State the blood parasite species.
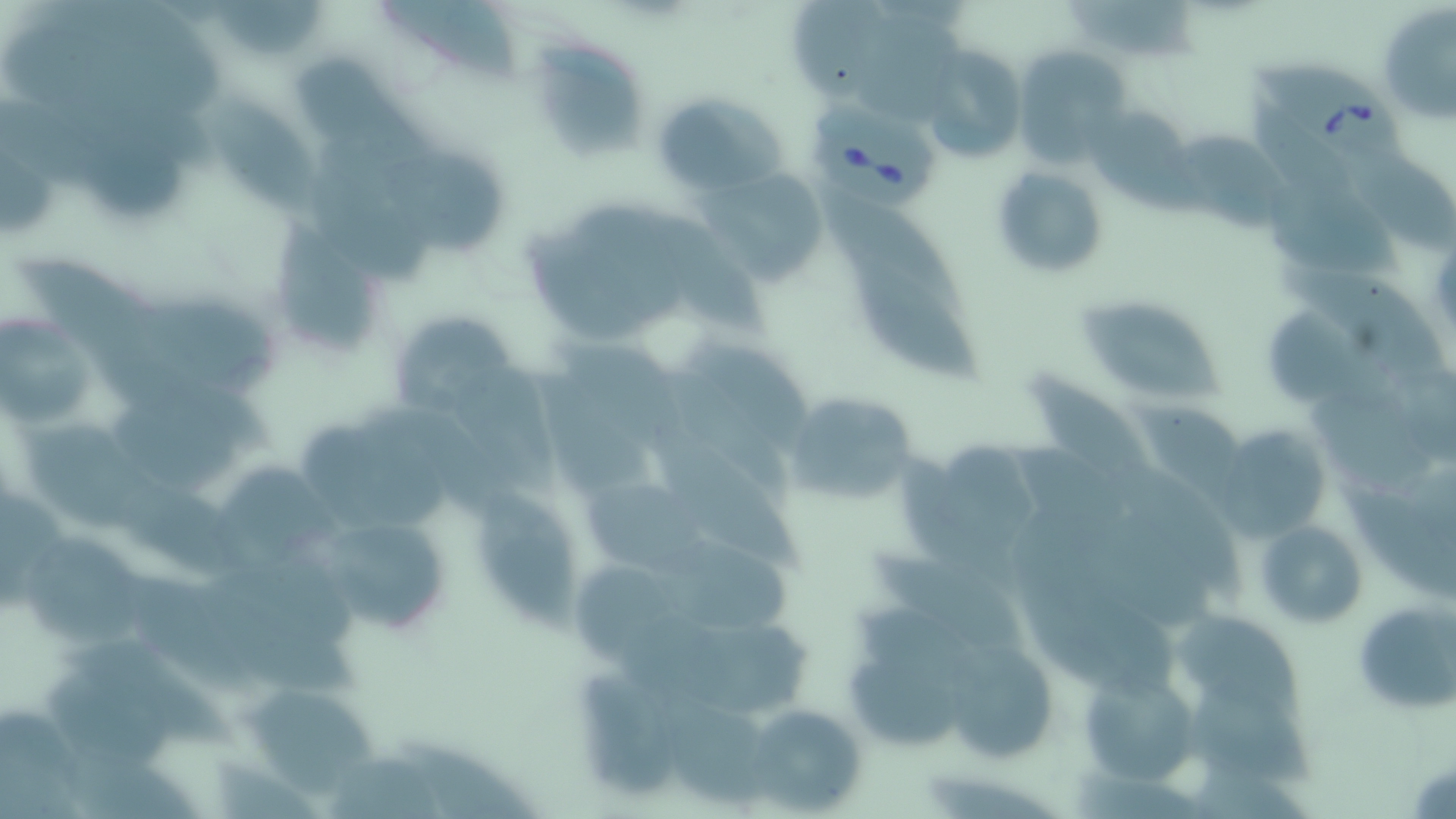

Babesia divergens.

Approximate bounding boxes as (x1, y1, x2, y2) in pixels. Uninfected red blood cell locations: (213, 0, 327, 59), (379, 0, 517, 86), (787, 0, 905, 107), (1377, 4, 1456, 127), (530, 37, 646, 162), (1013, 45, 1127, 160), (919, 46, 1023, 163), (205, 84, 320, 218), (651, 91, 786, 197), (1086, 105, 1190, 203), (1173, 133, 1299, 233), (377, 153, 512, 255), (992, 165, 1108, 279), (704, 166, 829, 284), (1258, 167, 1405, 281), (830, 194, 971, 315), (568, 196, 686, 327), (273, 214, 370, 357), (851, 256, 987, 387), (1284, 265, 1451, 389), (1079, 295, 1222, 404), (129, 297, 287, 409), (383, 309, 527, 421), (0, 314, 97, 433), (1024, 366, 1160, 512), (534, 370, 653, 496), (1312, 385, 1447, 500), (785, 392, 923, 510), (27, 419, 177, 539), (645, 423, 803, 580), (1212, 424, 1333, 547), (303, 426, 456, 524), (216, 457, 342, 578), (1334, 471, 1456, 606), (580, 477, 715, 575), (485, 485, 582, 638), (315, 510, 454, 636), (1256, 519, 1367, 628), (21, 535, 149, 649), (654, 541, 803, 633), (866, 545, 1035, 664), (184, 580, 361, 700), (1353, 596, 1455, 715), (1176, 615, 1306, 723), (946, 641, 1054, 763), (48, 658, 192, 774), (847, 659, 973, 752), (1081, 662, 1204, 787), (574, 670, 678, 798), (239, 682, 390, 798), (1189, 692, 1329, 790), (732, 699, 873, 816), (326, 752, 448, 819). Babesia divergens-infected red blood cell locations: (1248, 51, 1418, 178), (814, 100, 943, 210). Image is 1456×819 pixels. One field of a larger specimen. Light microscopy. May-Grünwald-Giemsa-stained preparation. Thin blood film. 1000x magnification.